Assess this cell for malaria.
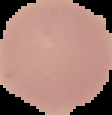

Uninfected.

image size = 112×115 pixels
image type = segmented cell region on a black background
preparation = thin blood smear